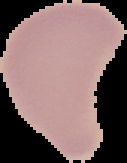
Summary:
  - Image type: segmented cell region with the area outside set to black
  - Preparation: thin blood smear
  - Result: no malaria parasites seen
  - Image size: 127×163 pixels